Report the malaria status of this cell.
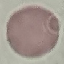
Uninfected.

stain = Giemsa
capture = smartphone through the microscope eyepiece
preparation = thin blood film
image type = automatically extracted cell patch, resized to 64 × 64 pixels